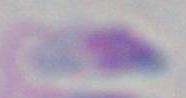

Summary:
  - Magnification: 1000x
  - Identification: Toxoplasma gondii
  - Modality: micrograph